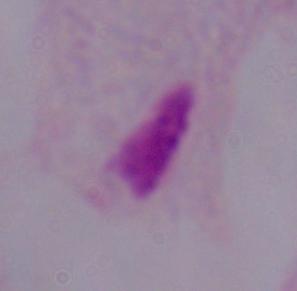 Photomicrograph. 1000x magnification. A trichomonad is shown.